Identify the cell.
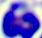
This is a leukocyte.

Summary:
  - Magnification: 400x
  - Modality: micrograph